Name the parasite shown.
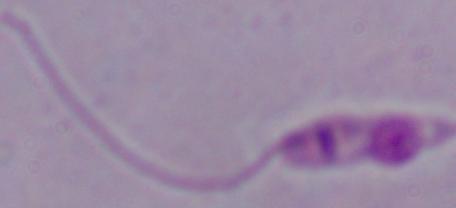
This is Leishmania.

Summary:
  - Magnification: 1000x
  - Modality: photomicrograph